Report the malaria status of this cell.
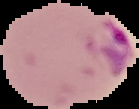
Parasitized.

From a thin blood smear. Segmented cell region on a black background. Image is 139×109 pixels.